Locate and identify every blood parasite.
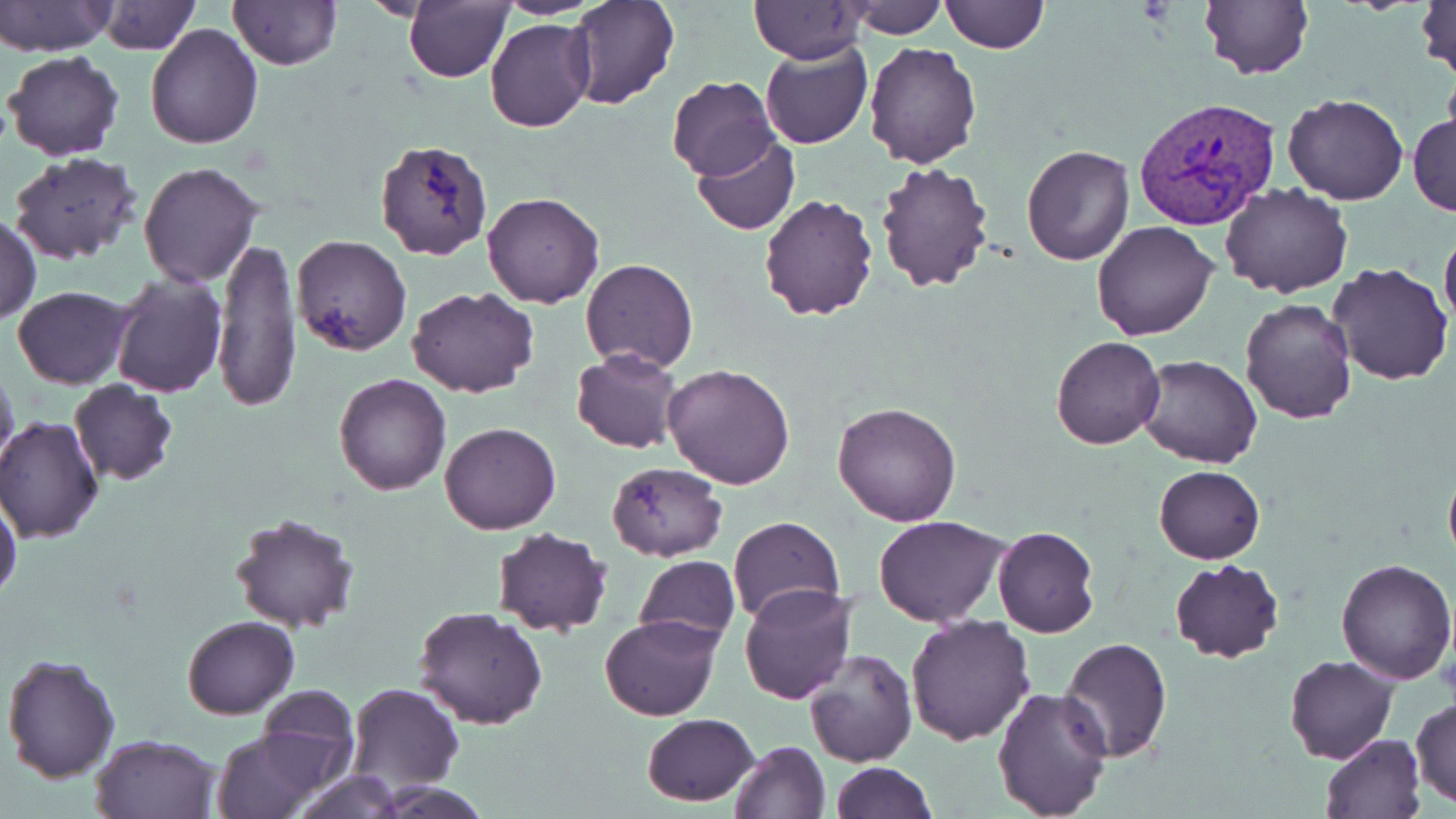

Approximate bounding boxes as (x1, y1, x2, y2) in pixels.
Plasmodium vivax-infected red blood cells: (1134, 96, 1280, 232).
No Plasmodium falciparum, Plasmodium ovale, Plasmodium malariae, Babesia divergens, or Trypanosoma brucei observed.

Uninfected red blood cell locations: (0, 0, 117, 56), (497, 0, 602, 18), (569, 0, 679, 108), (1416, 0, 1455, 83), (96, 1, 198, 54), (229, 1, 341, 70), (845, 1, 946, 39), (941, 1, 1051, 52), (1197, 1, 1314, 81), (404, 2, 512, 82), (749, 2, 867, 64), (485, 17, 594, 132), (145, 23, 264, 148), (760, 41, 870, 150), (863, 42, 982, 168), (5, 51, 126, 161), (667, 76, 780, 182), (1281, 94, 1409, 205), (1408, 111, 1456, 217), (691, 135, 799, 235), (375, 142, 491, 262), (1021, 144, 1134, 266), (7, 151, 146, 266), (875, 161, 996, 293), (138, 163, 263, 287), (1221, 184, 1352, 297), (481, 191, 605, 308), (758, 191, 879, 321), (1, 213, 40, 324), (1092, 220, 1219, 340), (1440, 225, 1456, 338), (291, 235, 412, 355), (214, 238, 300, 410), (581, 257, 699, 373), (1327, 263, 1453, 386), (109, 268, 227, 396), (13, 285, 134, 390), (407, 286, 540, 398), (1239, 297, 1357, 425), (1049, 336, 1166, 450), (571, 350, 681, 453), (1135, 355, 1262, 469), (662, 363, 796, 489), (0, 366, 20, 478), (334, 373, 452, 494), (69, 380, 177, 487), (832, 400, 962, 525), (0, 419, 103, 543), (440, 421, 560, 534), (1443, 458, 1456, 573), (606, 461, 728, 561), (1153, 464, 1264, 564), (0, 498, 22, 602), (229, 512, 361, 632), (873, 514, 1010, 625), (727, 516, 845, 624), (992, 524, 1100, 637), (490, 527, 614, 637), (634, 555, 739, 651), (1170, 558, 1283, 664), (1336, 558, 1455, 685), (739, 584, 857, 703), (414, 606, 548, 730), (599, 614, 723, 722), (906, 614, 1036, 745), (182, 615, 299, 719), (1059, 638, 1172, 762), (803, 648, 918, 766), (1, 653, 120, 785), (1285, 654, 1398, 763), (347, 682, 464, 794), (991, 685, 1112, 819), (253, 686, 360, 785), (1411, 697, 1456, 809), (642, 714, 760, 805), (211, 729, 321, 818), (91, 734, 221, 819), (1320, 734, 1425, 819), (728, 739, 829, 819), (830, 761, 936, 819), (290, 770, 405, 819). Platelet locations: (1438, 651, 1456, 701). Slide-level diagnosis: Plasmodium vivax. Captured at 1000x magnification. Single field of view. Thin blood smear. Image is 1456×819 pixels. May-Grünwald-Giemsa-stained preparation. Optical microscopy.